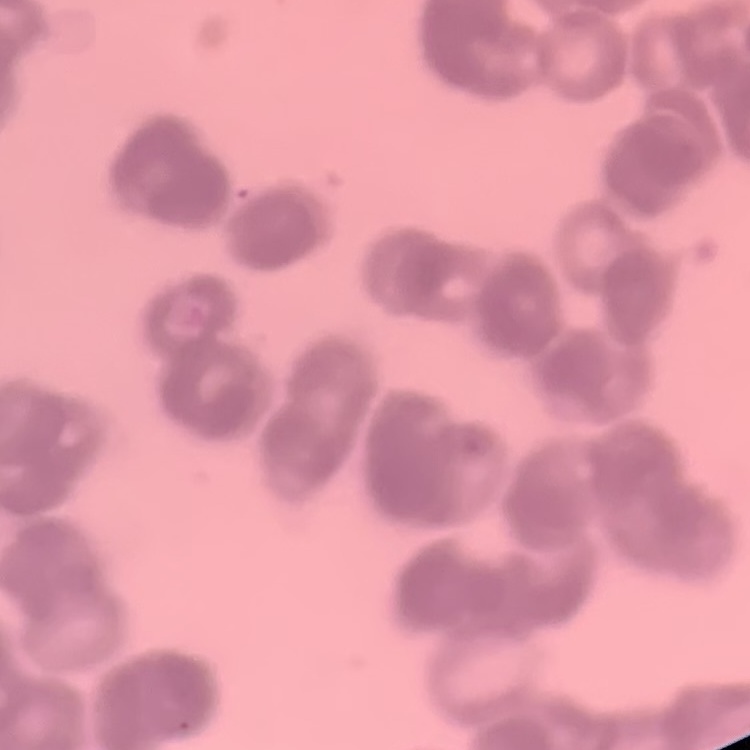
Summary:
  - Red blood cell morphology: rouleaux formation
  - Image type: one tile cut from a larger photomicrograph
  - Stain: Field's or Giemsa
  - Preparation: thin blood smear